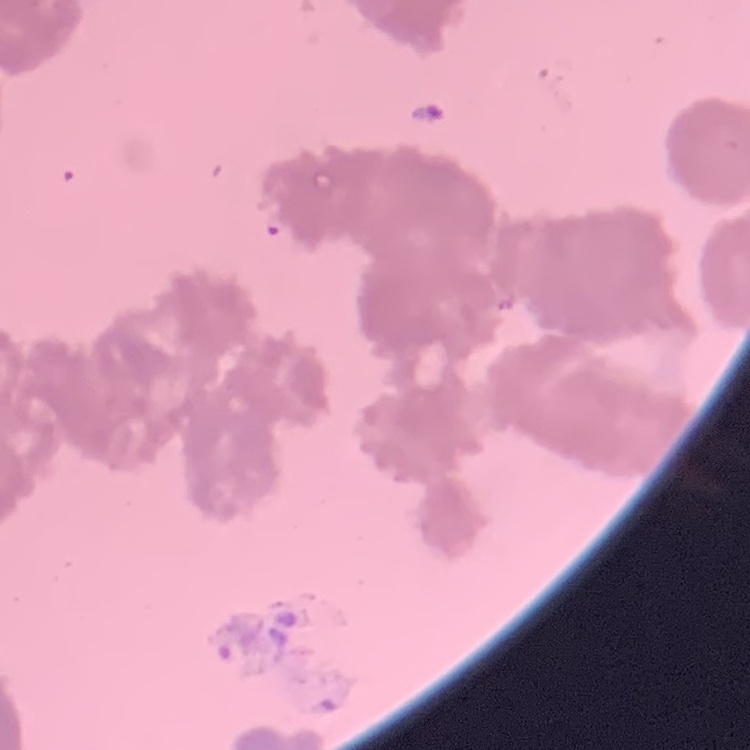
erythrocyte morphology = rouleaux formation
preparation = thin blood film
image type = square crop of a larger photomicrograph
stain = Field's or Giemsa